Outline each blood parasite and name the species.
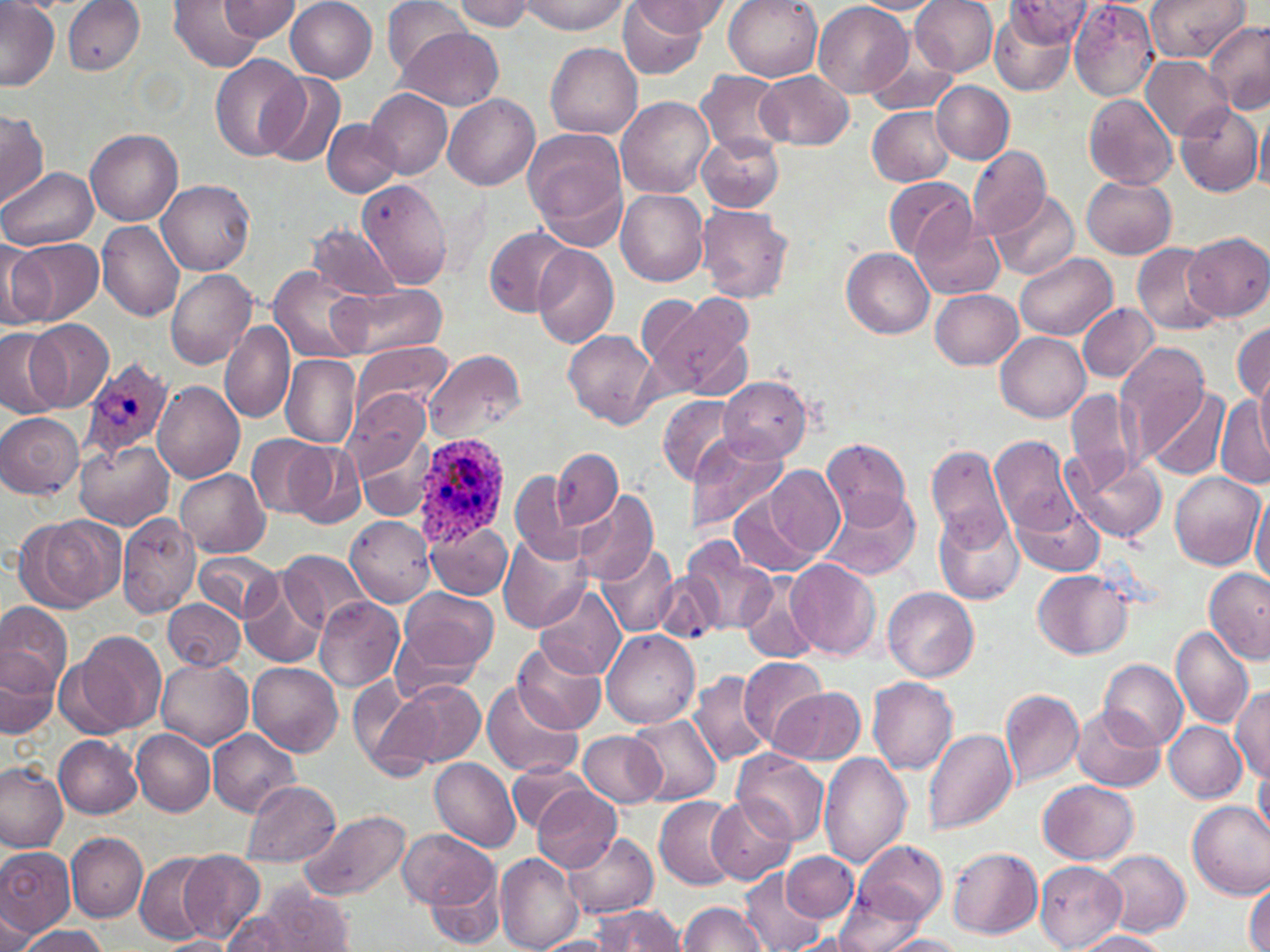
Approximate bounding boxes as (x1, y1, x2, y2) in pixels.
Plasmodium ovale-infected red blood cells: (81, 358, 173, 464), (409, 431, 516, 545).
No Plasmodium falciparum, Plasmodium malariae, Plasmodium vivax, Babesia divergens, or Trypanosoma brucei observed.

slide_level_diagnosis: Plasmodium ovale
uninfected_red_blood_cell_locations: 'approximate bounding boxes as (x1, y1, x2, y2) in pixels: (0, 0, 59, 90), (220, 0, 302, 42), (285, 0, 378, 83), (382, 0, 469, 75), (451, 0, 536, 32), (520, 0, 630, 34), (724, 0, 821, 81), (911, 0, 999, 77), (1069, 0, 1160, 102), (1145, 0, 1248, 60), (171, 1, 265, 72), (625, 1, 725, 39), (849, 1, 948, 14), (1004, 1, 1095, 46), (62, 2, 145, 76), (617, 2, 710, 80), (813, 2, 913, 99), (990, 5, 1078, 96), (1204, 21, 1270, 115), (398, 28, 503, 110), (546, 44, 642, 138), (865, 50, 954, 115), (209, 53, 308, 159), (1140, 56, 1232, 140), (697, 69, 790, 156), (755, 69, 855, 150), (258, 72, 347, 167), (932, 81, 1014, 163), (367, 89, 452, 180), (1085, 92, 1178, 190), (444, 94, 539, 191), (617, 96, 714, 199), (1174, 101, 1262, 196), (1256, 105, 1270, 194), (0, 106, 49, 210), (867, 106, 955, 186), (323, 119, 400, 196), (523, 127, 628, 242), (86, 129, 183, 227), (696, 130, 783, 212), (967, 145, 1051, 239), (1, 167, 97, 251), (1083, 175, 1177, 259), (357, 177, 456, 289), (883, 177, 972, 261), (157, 178, 254, 274), (990, 188, 1081, 279), (616, 190, 708, 287), (697, 205, 793, 303), (911, 213, 1006, 301), (97, 221, 185, 321), (303, 222, 402, 301), (484, 226, 576, 316), (1186, 233, 1269, 320), (8, 237, 103, 324), (2, 239, 50, 330), (1131, 242, 1223, 335), (531, 246, 618, 347), (840, 247, 934, 339), (1016, 253, 1118, 339), (269, 267, 373, 363), (166, 269, 258, 369), (332, 282, 449, 358), (929, 288, 1023, 369), (637, 293, 713, 382), (657, 293, 753, 396), (1078, 302, 1158, 384), (25, 318, 114, 412), (1232, 322, 1270, 402), (219, 323, 295, 422), (0, 327, 69, 416), (563, 329, 658, 429), (996, 332, 1090, 421), (352, 342, 453, 419), (1115, 344, 1214, 464), (423, 349, 527, 440), (281, 355, 361, 447), (1254, 359, 1270, 452), (718, 377, 812, 465), (152, 381, 244, 484), (1142, 386, 1231, 479), (1065, 388, 1140, 489), (345, 389, 432, 480), (1215, 390, 1270, 490), (659, 395, 738, 484), (0, 411, 84, 499), (246, 435, 335, 519), (685, 435, 789, 535), (992, 435, 1083, 537), (357, 437, 433, 521), (822, 439, 911, 529), (74, 440, 173, 531), (287, 444, 366, 528), (927, 444, 1010, 548), (552, 447, 622, 528), (1065, 453, 1168, 545), (766, 466, 845, 557), (176, 469, 270, 558), (1169, 470, 1264, 570), (511, 472, 581, 561), (574, 488, 658, 583), (820, 492, 921, 582), (729, 494, 819, 577), (1251, 494, 1270, 589), (1010, 496, 1105, 578), (934, 509, 1022, 605), (117, 512, 202, 617), (23, 515, 123, 611), (347, 515, 435, 607), (425, 522, 513, 598), (500, 533, 592, 632), (680, 537, 777, 636), (597, 542, 679, 638), (279, 549, 372, 631), (194, 551, 281, 623), (787, 559, 880, 660), (1202, 566, 1269, 662), (1031, 569, 1132, 660), (654, 573, 723, 643), (740, 575, 818, 664), (242, 576, 327, 669), (533, 583, 627, 680), (399, 587, 498, 671), (883, 587, 978, 681), (314, 597, 404, 692), (162, 598, 244, 669), (0, 604, 71, 701), (391, 621, 489, 705), (1171, 624, 1255, 730), (602, 629, 700, 728), (62, 630, 167, 737), (1, 640, 62, 737), (512, 640, 607, 736), (739, 655, 829, 748), (154, 656, 252, 749), (1100, 660, 1187, 751), (248, 662, 342, 755), (689, 669, 771, 768), (347, 677, 422, 770), (370, 677, 486, 775), (868, 677, 958, 775), (482, 680, 581, 779), (1231, 685, 1270, 784), (771, 687, 865, 764), (1000, 688, 1085, 788), (1073, 707, 1164, 791), (1200, 707, 1269, 794), (627, 715, 721, 807), (1164, 721, 1247, 801), (207, 728, 301, 816), (923, 728, 1017, 835), (131, 729, 214, 816), (579, 731, 668, 807), (56, 736, 142, 817), (733, 751, 830, 845), (817, 754, 912, 871), (430, 757, 521, 851), (508, 760, 586, 833), (0, 761, 68, 851), (1253, 768, 1269, 843), (243, 779, 342, 865), (1039, 779, 1139, 863), (531, 785, 621, 874), (654, 795, 742, 889), (707, 795, 795, 884), (1186, 800, 1270, 899), (298, 809, 413, 903), (398, 828, 498, 912), (564, 831, 659, 920), (67, 833, 147, 921), (847, 841, 948, 927), (0, 846, 76, 937), (947, 847, 1042, 939), (782, 849, 859, 922), (178, 850, 265, 942), (1098, 850, 1190, 938), (134, 851, 217, 944), (495, 852, 584, 952), (1035, 860, 1126, 951), (741, 866, 827, 952), (417, 867, 503, 947), (1245, 878, 1270, 952), (252, 884, 357, 952), (833, 887, 933, 952), (678, 901, 768, 952), (591, 904, 686, 951), (219, 905, 322, 951), (0, 909, 36, 950), (17, 925, 112, 952), (1070, 931, 1173, 952), (879, 934, 970, 952), (155, 936, 239, 951), (535, 936, 616, 952)'
image_size: 1270×952 pixels
stain: May-Grünwald-Giemsa
preparation: thin blood smear
modality: optical microscopy
magnification: 1000x
field_of_view: single